Report the malaria status of this cell.
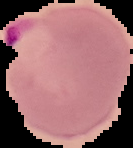
Parasitized.

Summary:
  - Image size: 133×148 pixels
  - Image type: segmented cell region on a black background
  - Preparation: thin blood smear